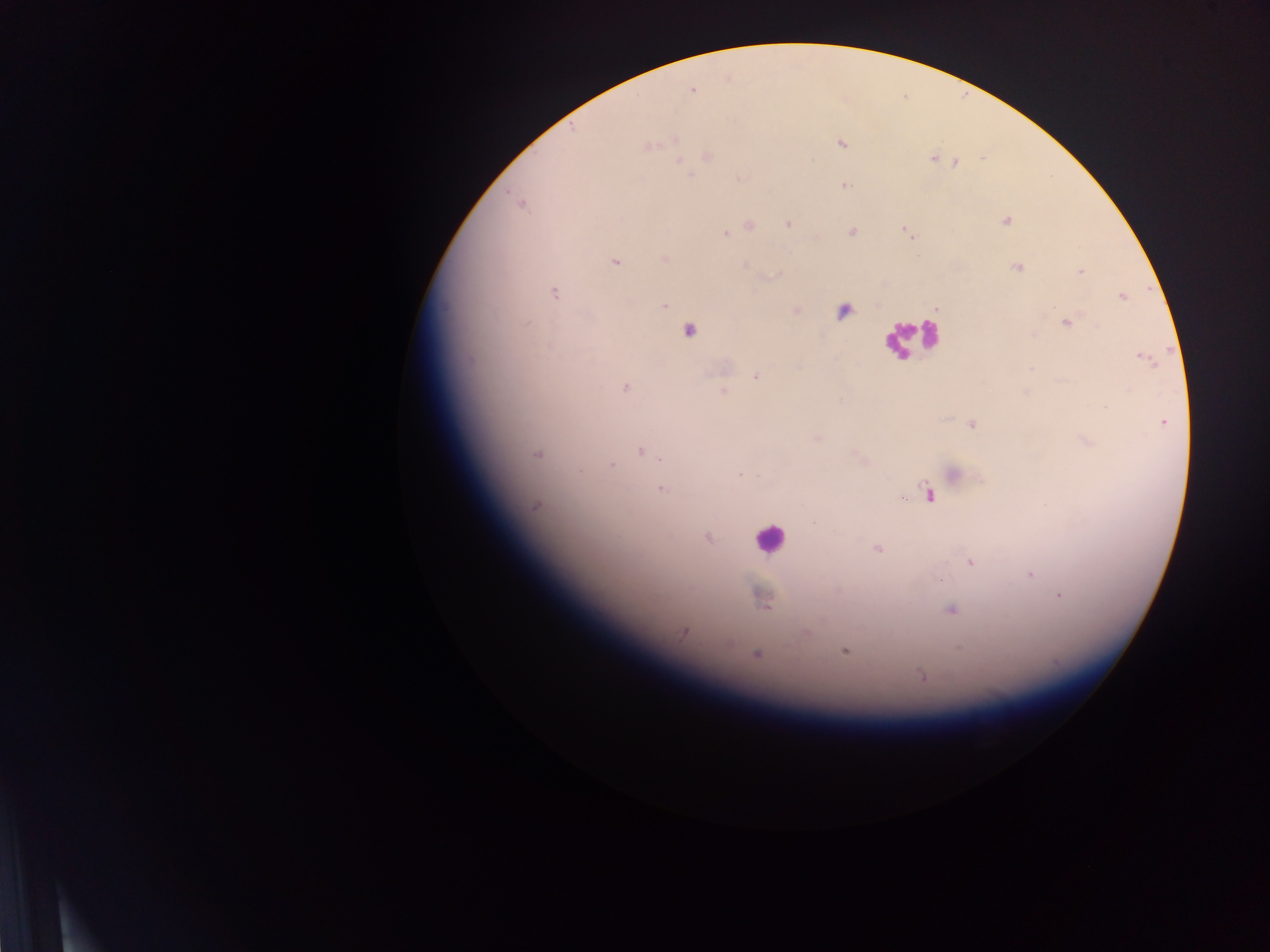
Approximate centers as x y in pixels.
Summary:
  - Plasmodium parasite locations: 692 89; 674 140; 841 144; 647 147; 707 156; 933 158; 679 162; 954 163; 844 185; 520 202; 1005 220; 789 224; 748 225; 731 230; 905 231; 851 232; 724 233; 664 259; 614 261; 1018 266; 1081 271; 552 292; 1122 296; 663 305; 936 308; 795 310; 842 311; 1067 321; 689 329; 1141 357; 757 376; 625 386; 723 391; 1105 407; 1162 422; 972 423; 817 438; 641 450; 537 453; 611 464; 739 473; 954 474; 661 488; 929 494; 535 506; 708 537; 877 549; 970 562; 1028 574; 939 580; 1060 596; 762 598; 951 609; 684 631; 806 632; 845 651; 756 654; 923 676
  - Leukocyte locations: 912 339; 769 538
  - Image size: 1270×952 pixels
  - Field of view: single
  - Preparation: thick blood film
  - Country: Ghana
  - Capture: mobile-phone photograph through a microscope